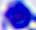
Summary:
  - Magnification: 400x
  - Modality: micrograph
  - Identification: white blood cell